Point out each Plasmodium parasite.
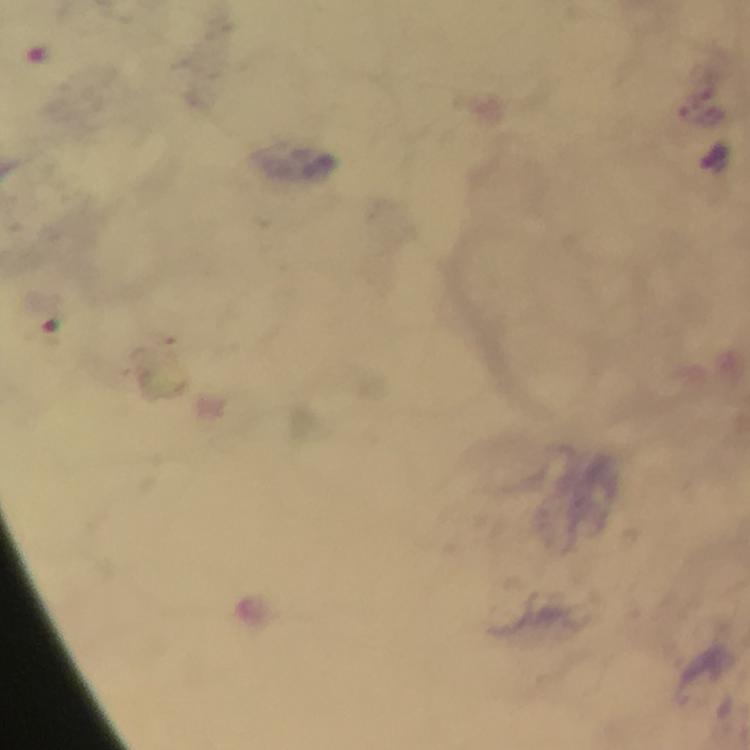

Approximate centers as (x, y) in pixels.
Plasmodium parasites: (702, 116).

Summary:
  - Cropped from: one field of view
  - Immersion oil: used
  - Context: from a diagnostic examination for malaria
  - Magnification: 100x
  - Stain: Giemsa
  - Preparation: thick blood smear
  - Image size: 750×750 pixels
  - Capture: smartphone camera through the microscope